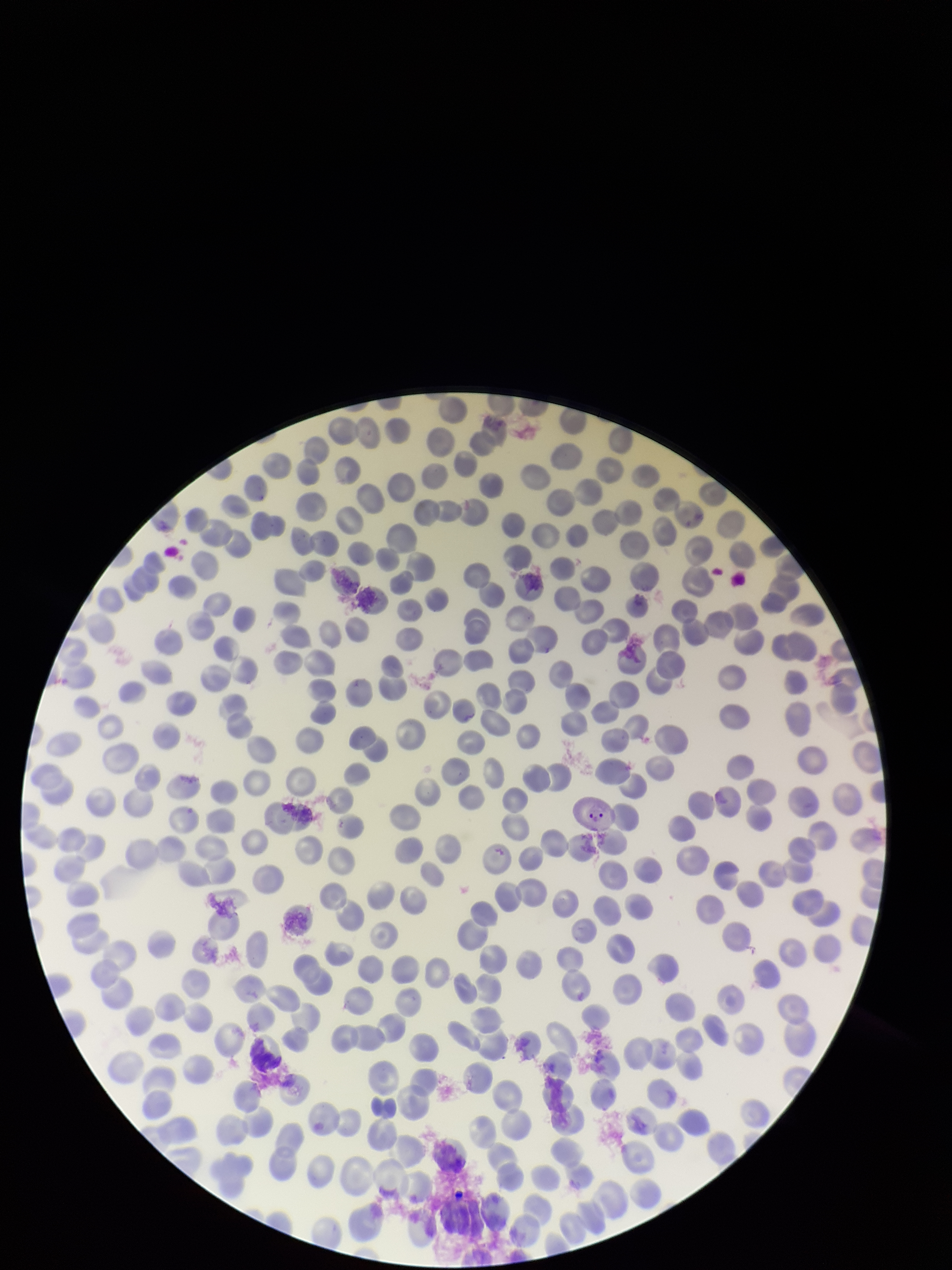

Parasitized red blood cells: detected. Parasitized red blood cell count: 1. Image is 952×1270 pixels. Smartphone photograph taken through the eyepiece of a microscope. One field from this slide. Patient malaria status: positive. Stained with Giemsa. Preparation: thin blood smear. Red blood cell count: 299. Species reported for this patient: Plasmodium vivax.